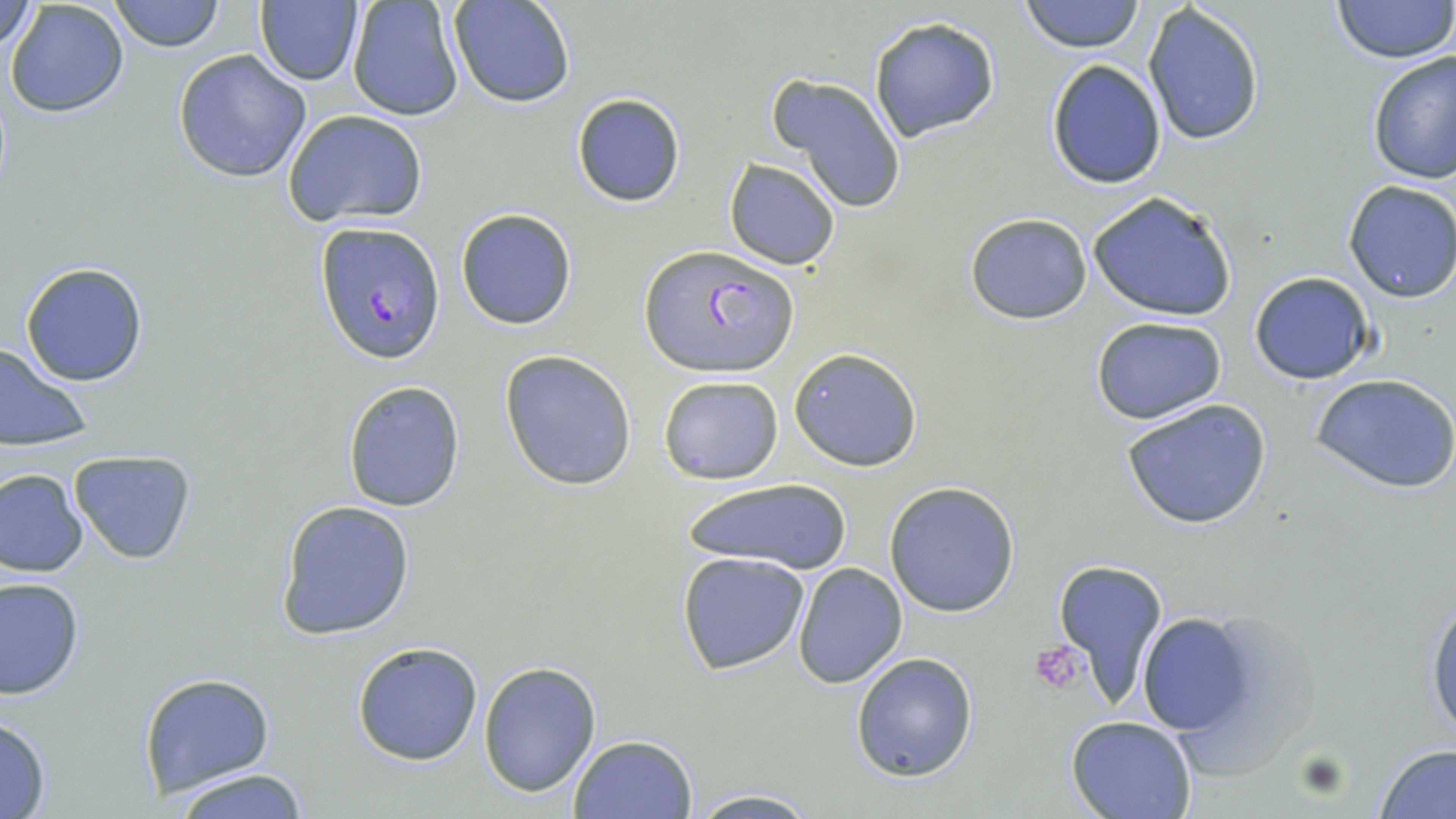

Summary:
  - Coordinate format: approximate bounding boxes as [x1, y1, x2, y2] in pixels
  - Platelet locations: [1031, 642, 1089, 693]
  - Uninfected red blood cell locations: [107, 0, 226, 52], [448, 0, 577, 109], [1021, 0, 1143, 53], [1333, 1, 1452, 63], [1, 2, 39, 54], [4, 2, 130, 117], [254, 2, 363, 86], [346, 2, 463, 122], [1143, 3, 1267, 147], [869, 18, 1000, 140], [173, 48, 312, 183], [1365, 49, 1456, 187], [1046, 59, 1166, 188], [768, 74, 907, 213], [571, 93, 686, 207], [282, 109, 428, 228], [724, 159, 843, 270], [1343, 180, 1456, 303], [1086, 190, 1239, 322], [455, 208, 578, 330], [965, 212, 1092, 325], [19, 261, 150, 387], [1250, 273, 1375, 385], [1090, 316, 1227, 423], [0, 342, 92, 453], [789, 346, 925, 471], [499, 349, 637, 491], [1311, 371, 1456, 494], [658, 375, 784, 485], [341, 379, 465, 512], [1122, 398, 1272, 531], [69, 451, 197, 565], [0, 467, 88, 577], [678, 476, 859, 578], [882, 481, 1022, 617], [276, 500, 415, 640], [675, 553, 809, 676], [1051, 558, 1169, 711], [791, 562, 908, 686], [1, 576, 83, 700], [1425, 584, 1456, 745], [1133, 607, 1268, 745], [352, 640, 483, 765], [850, 651, 979, 780], [477, 661, 602, 796], [138, 672, 275, 798], [0, 714, 53, 819], [1067, 716, 1198, 819], [567, 734, 697, 818], [1376, 746, 1456, 819], [163, 768, 317, 818], [685, 790, 826, 818]
  - Plasmodium falciparum-infected red blood cell locations: [314, 221, 445, 364], [640, 245, 799, 378]
  - Slide-level diagnosis: Plasmodium falciparum
  - Field of view: one of a larger specimen
  - Modality: optical microscopy
  - Image size: 1456×819 pixels
  - Preparation: thin blood smear
  - Magnification: 1000x
  - Stain: May-Grünwald-Giemsa